Assess the morphology of the erythrocytes.
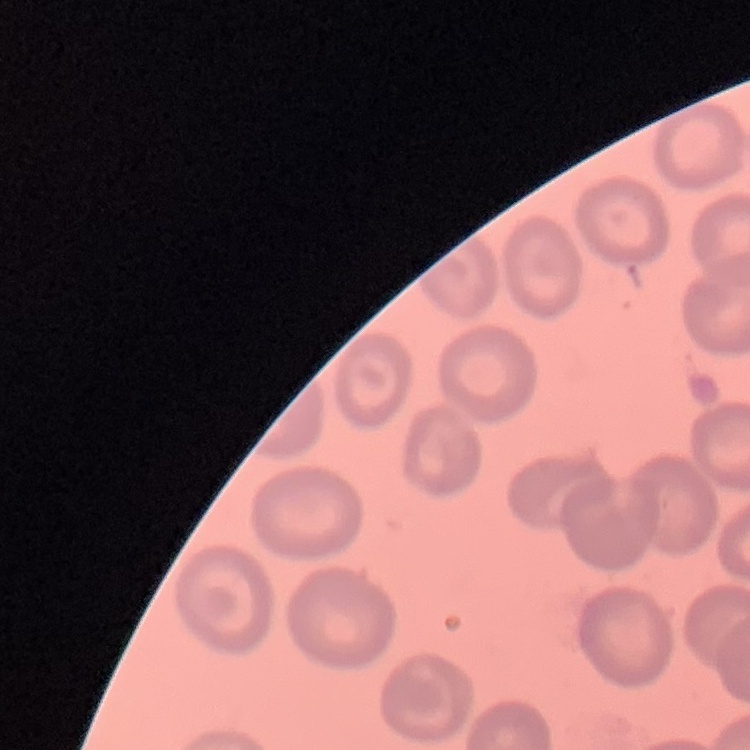

They show no rouleaux formation.

One tile cut from a larger photomicrograph. Thin blood smear. Stained with either Field's or Giemsa.